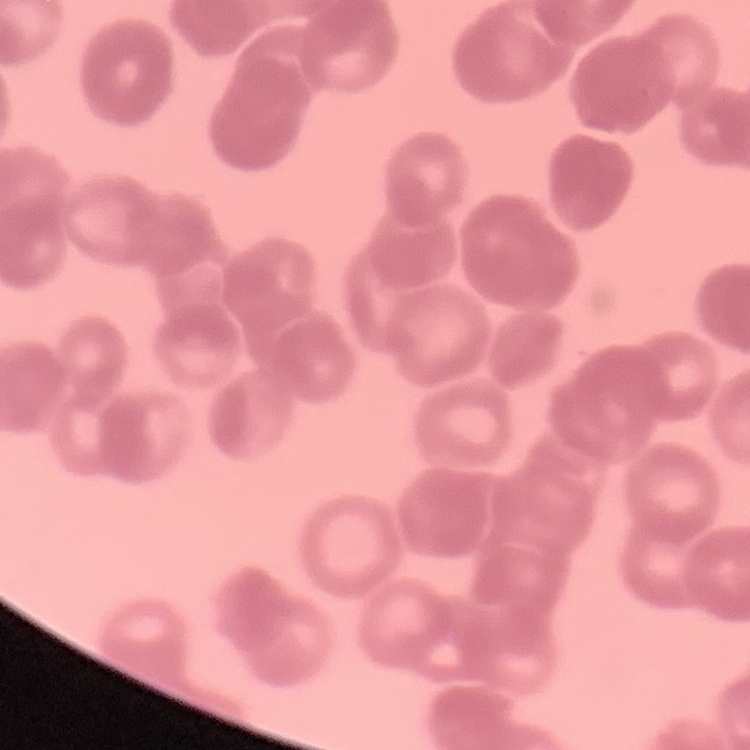
red blood cell morphology = rouleaux formation
preparation = thin blood smear
stain = Field's or Giemsa
image type = one tile cut from a larger photomicrograph